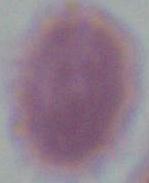

modality = micrograph
magnification = 1000x
identification = red blood cell